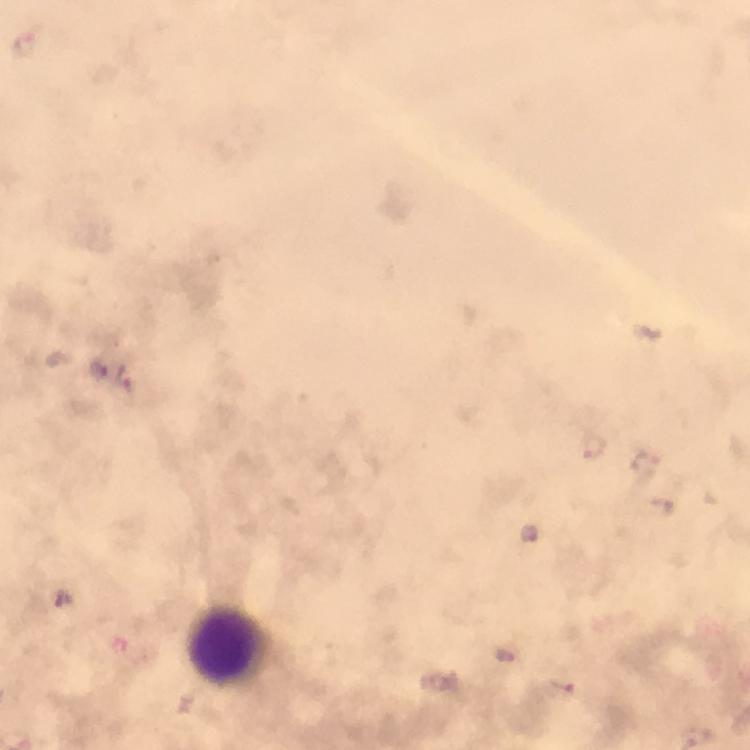 Approximate centers as (x, y) in pixels. Leukocyte locations: (223, 644). Malaria parasite locations: (99, 368), (126, 380), (529, 533), (504, 655), (562, 686), (698, 737). From a diagnostic examination for malaria. Cropped region of a single field of view. 100x magnification. Thick blood film. Image is 750×750 pixels. Smartphone photograph taken through a microscope. Giemsa stain. Immersion oil was used.